Point out each malaria parasite.
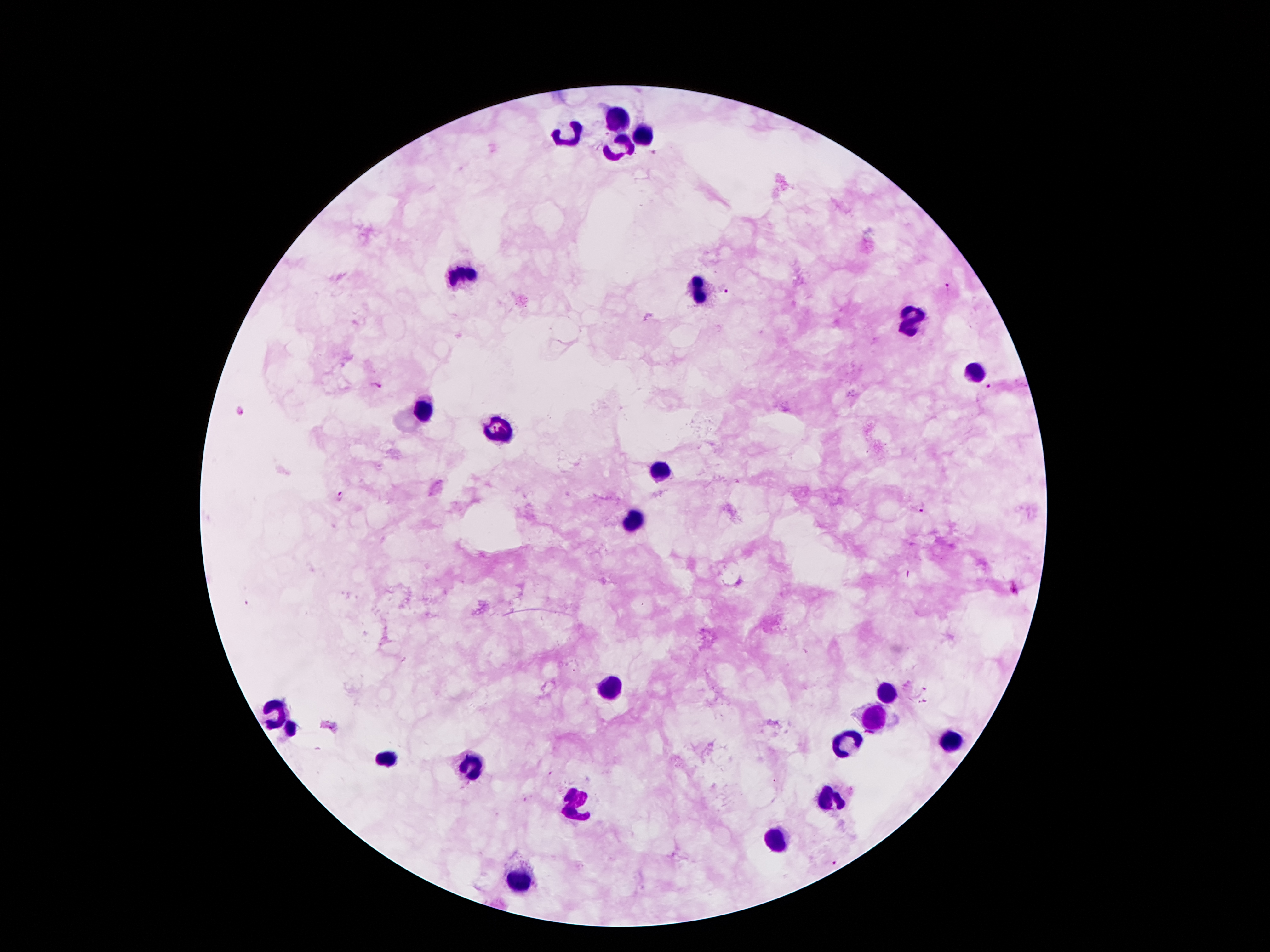

Approximate centers as (x, y) in pixels.
Malaria parasites: (652, 153), (946, 288), (725, 290), (374, 385), (991, 386), (240, 413), (339, 497), (923, 508), (1014, 589), (925, 688), (921, 702), (837, 861).

leukocyte locations = (618, 120), (645, 134), (568, 136), (617, 146), (465, 270), (697, 293), (911, 320), (972, 370), (422, 409), (497, 430), (661, 472), (634, 523), (886, 693), (277, 713), (874, 720), (289, 729), (951, 743), (847, 745), (384, 761), (468, 764), (831, 797), (575, 804), (777, 845), (520, 881)
capture = smartphone through the microscope eyepiece
patient malaria status = positive for Plasmodium falciparum
magnification = 100x
stain = Giemsa
preparation = thick blood smear
image size = 1270×952 pixels
field of view = one from this slide